Give the position of every leukocyte visible.
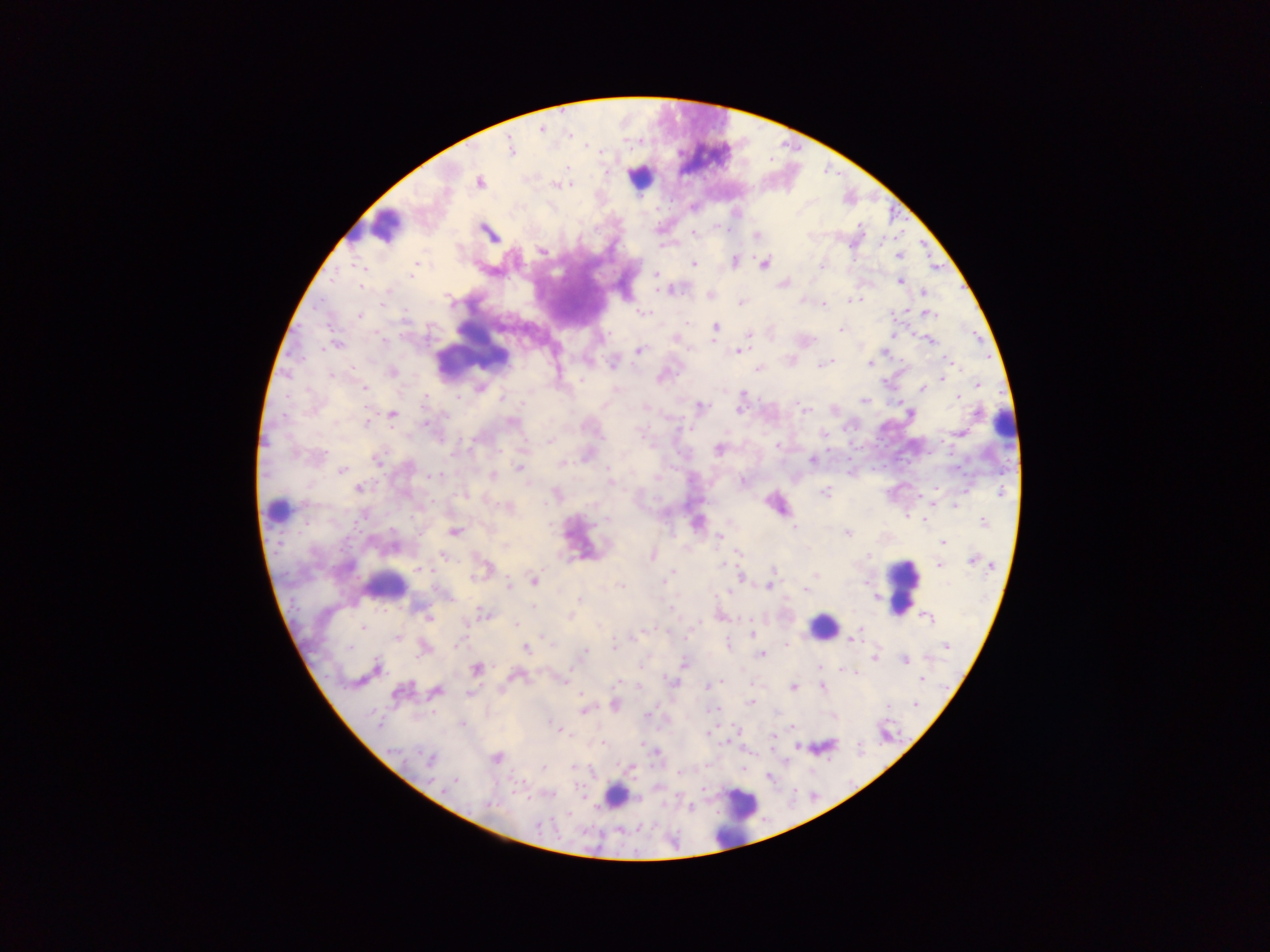
Approximate centers as x y in pixels.
Leukocytes: 705 156; 638 176; 385 226; 473 331; 1004 424; 277 510; 580 539; 384 586; 901 586; 822 626; 614 796; 741 805; 736 817.

capture = mobile-phone photograph through a microscope
country = Ghana
image size = 1270×952 pixels
preparation = thick blood film
Plasmodium parasite locations = approximate centers as x y in pixels: 541 129; 509 148; 479 182; 557 185; 488 232; 694 232; 756 235; 541 251; 899 256; 734 260; 764 262; 692 265; 415 268; 655 275; 899 280; 783 283; 671 289; 923 292; 709 294; 858 299; 803 300; 852 300; 741 302; 822 304; 382 305; 643 312; 925 312; 359 314; 716 327; 841 328; 749 334; 891 335; 675 338; 929 340; 336 344; 639 350; 739 352; 886 353; 790 359; 613 362; 950 362; 868 363; 822 365; 757 368; 392 372; 661 377; 941 377; 977 384; 364 387; 479 388; 922 388; 955 397; 503 398; 864 401; 605 406; 698 407; 645 408; 741 409; 804 409; 392 414; 511 422; 823 433; 961 433; 549 440; 719 449; 376 458; 812 460; 563 464; 520 468; 342 470; 492 475; 657 478; 609 481; 742 481; 359 488; 825 492; 462 495; 556 495; 931 501; 775 504; 955 504; 508 506; 606 519; 924 519; 983 522; 697 523; 794 528; 454 531; 846 533; 718 537; 942 542; 504 545; 736 551; 442 555; 653 555; 972 559; 939 565; 419 569; 484 569; 772 569; 815 574; 741 576; 664 580; 534 581; 621 584; 767 585; 728 590; 806 591; 446 596; 534 607; 483 614; 570 615; 427 616; 926 618; 515 623; 363 628; 751 635; 398 637; 545 637; 852 637; 946 645; 424 647; 526 648; 582 654; 761 654; 875 656; 904 660; 684 664; 376 668; 477 669; 818 670; 854 672; 516 675; 561 679; 922 679; 620 682; 672 682; 637 685; 708 686; 821 686; 792 687; 435 690; 399 692; 469 693; 582 694; 580 701; 751 702; 917 702; 613 703; 716 709; 583 710; 833 715; 647 716; 461 724; 559 728; 736 729; 708 732; 773 736; 726 742; 640 743; 655 751; 495 758; 430 760; 542 767; 630 767; 679 772; 456 781; 701 788
field of view = single